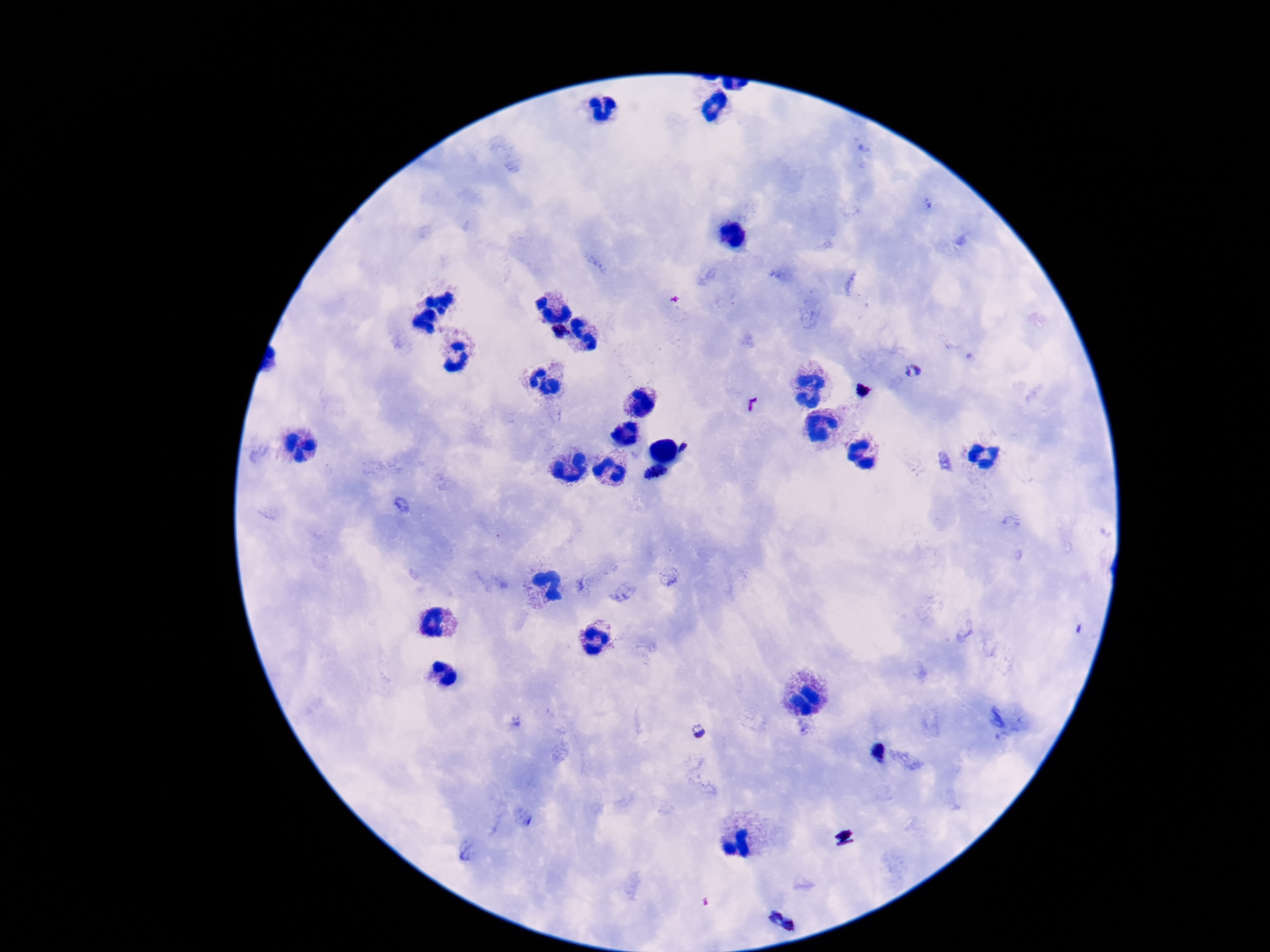
Approximate object centers, in pixels from the top-left corner. Plasmodium parasite locations: (x=560, y=333), (x=914, y=372), (x=752, y=405), (x=687, y=446), (x=655, y=474), (x=701, y=728), (x=878, y=756), (x=782, y=922). One field from this slide. Patient malaria status: positive. Thick blood film. 100x magnification. Image is 1270×952 pixels. Smartphone photograph taken through the microscope eyepiece. Giemsa stain.